Locate and identify every blood parasite.
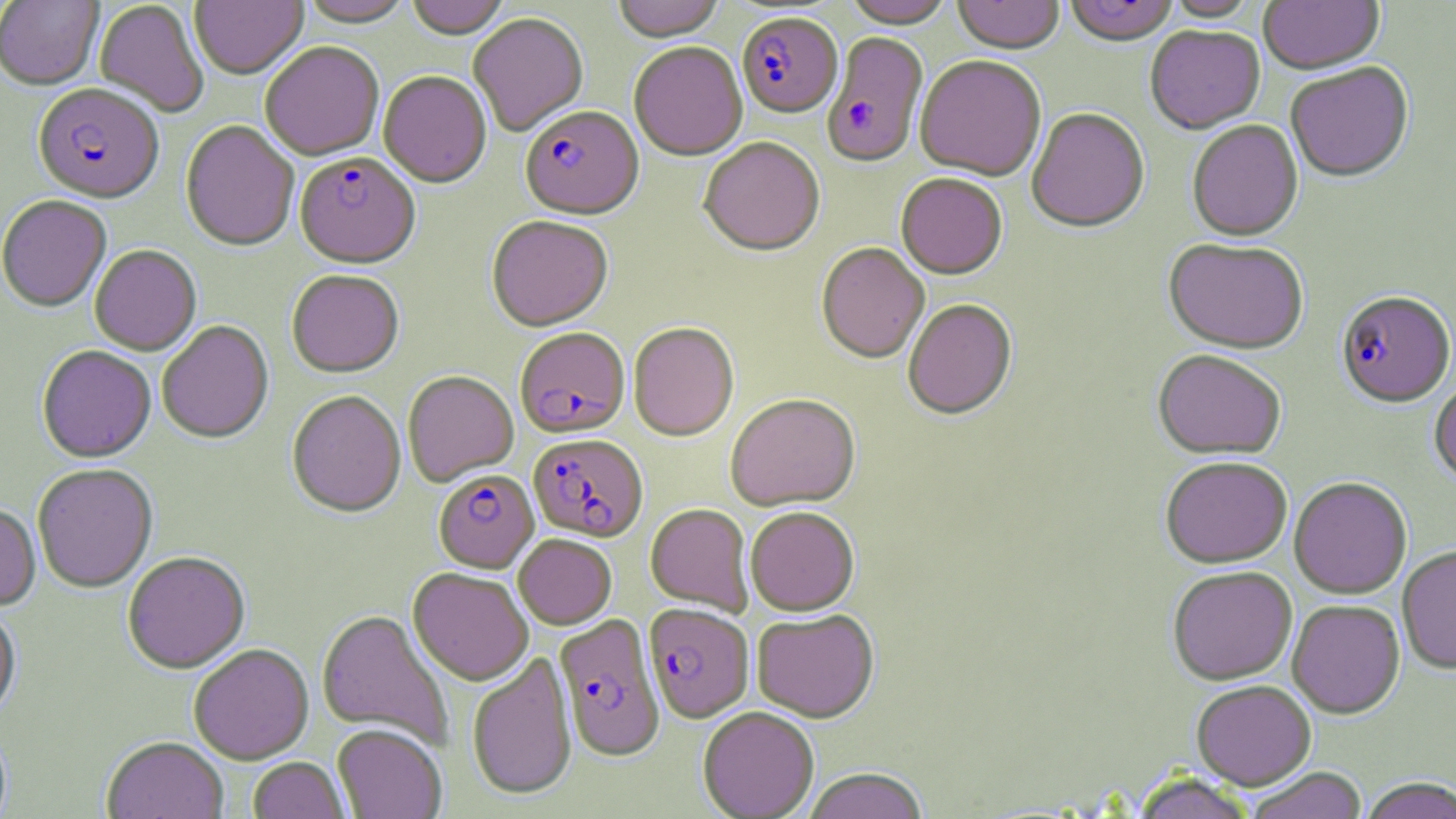

Approximate bounding boxes as (x1, y1, x2, y2) in pixels.
Plasmodium falciparum-infected red blood cells: (737, 14, 842, 120), (822, 34, 929, 171), (33, 85, 164, 206), (520, 107, 644, 221), (294, 153, 420, 270), (1336, 292, 1455, 409), (515, 329, 630, 439), (528, 434, 648, 542), (433, 470, 539, 572), (643, 604, 754, 722), (554, 614, 665, 762).
No Plasmodium ovale, Plasmodium malariae, Plasmodium vivax, Babesia divergens, or Trypanosoma brucei observed.

Summary:
  - Uninfected red blood cell locations: (190, 0, 307, 81), (405, 0, 510, 40), (612, 0, 726, 43), (841, 0, 956, 30), (952, 0, 1065, 56), (1063, 0, 1179, 48), (1, 1, 103, 91), (95, 1, 209, 118), (297, 1, 415, 29), (1163, 1, 1262, 23), (1258, 1, 1385, 77), (468, 14, 588, 138), (1145, 26, 1265, 135), (260, 44, 384, 163), (629, 44, 748, 162), (914, 57, 1047, 183), (1286, 63, 1414, 184), (377, 73, 491, 189), (1027, 109, 1149, 234), (181, 121, 299, 253), (1187, 121, 1303, 241), (699, 139, 825, 258), (896, 174, 1007, 280), (0, 197, 111, 314), (486, 217, 613, 332), (1163, 239, 1309, 354), (816, 243, 929, 365), (90, 246, 202, 356), (286, 270, 404, 379), (903, 300, 1017, 421), (156, 321, 274, 445), (629, 323, 739, 443), (37, 346, 156, 464), (1153, 349, 1286, 460), (403, 371, 519, 487), (1430, 379, 1456, 485), (287, 392, 406, 519), (725, 394, 861, 511), (1160, 456, 1292, 568), (33, 465, 158, 594), (1289, 477, 1412, 599), (645, 503, 753, 616), (0, 505, 41, 612), (745, 506, 860, 616), (513, 534, 617, 630), (1397, 546, 1456, 675), (123, 553, 250, 674), (1167, 567, 1297, 686), (408, 568, 533, 686), (1287, 600, 1405, 719), (0, 604, 21, 723), (316, 610, 454, 749), (751, 610, 880, 723), (188, 644, 314, 765), (466, 653, 577, 802), (1191, 680, 1316, 790), (697, 706, 819, 818), (332, 725, 446, 819), (102, 738, 228, 819), (248, 757, 350, 819), (802, 768, 929, 819), (1245, 768, 1368, 819), (1129, 773, 1259, 819), (1358, 778, 1456, 819)
  - Slide-level diagnosis: Plasmodium falciparum
  - Image size: 1456×819 pixels
  - Field of view: single
  - Stain: May-Grünwald-Giemsa
  - Modality: light microscopy
  - Magnification: 1000x
  - Preparation: thin blood smear